Name the parasite shown.
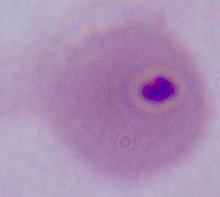
Plasmodium.

Summary:
  - Modality: micrograph
  - Magnification: 400x or 1000x